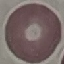

malaria status = uninfected
image type = automatically extracted cell patch, resized to 64 × 64 pixels
preparation = thin blood film
capture = smartphone camera at the microscope eyepiece
stain = Giemsa